Name the blood parasite species.
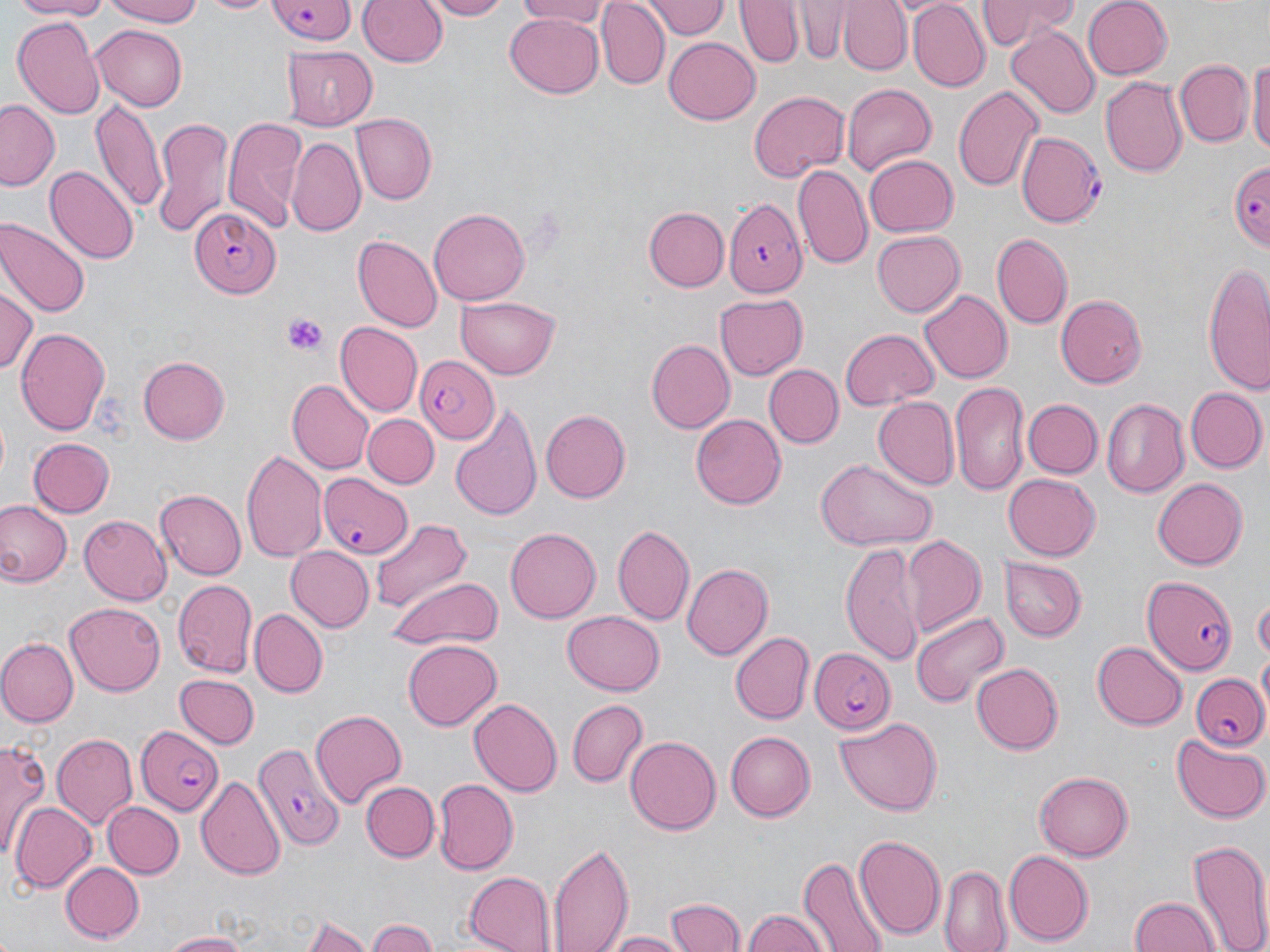
Plasmodium falciparum.

Summary:
  - Coordinate format: approximate bounding boxes as (x1,y1)-(x2,y2) corner pairs in pixels
  - Plasmodium falciparum-infected red blood cell locations: (262,2)-(357,44), (1018,131)-(1106,230), (1225,158)-(1267,252), (727,198)-(808,298), (189,207)-(279,295), (414,355)-(499,444), (319,474)-(413,558), (1144,575)-(1235,674), (807,649)-(895,731), (1189,671)-(1270,750), (136,724)-(225,815), (251,737)-(343,848)
  - Platelet locations: (282,313)-(330,356)
  - Uninfected red blood cell locations: (7,0)-(113,19), (101,0)-(208,26), (196,0)-(276,14), (358,0)-(448,70), (421,0)-(515,20), (514,0)-(616,26), (647,0)-(729,42), (735,0)-(803,68), (839,0)-(913,75), (976,0)-(1078,49), (1080,0)-(1172,81), (907,1)-(989,91), (787,3)-(854,62), (598,4)-(668,88), (506,11)-(604,96), (12,14)-(105,117), (92,23)-(187,109), (1007,26)-(1099,119), (663,38)-(760,124), (282,46)-(374,128), (1248,51)-(1270,165), (1174,59)-(1254,147), (1101,76)-(1188,176), (841,83)-(937,174), (953,83)-(1043,195), (750,90)-(847,184), (91,99)-(165,216), (0,101)-(62,191), (352,115)-(437,203), (222,116)-(307,232), (150,117)-(233,237), (287,137)-(366,238), (865,156)-(959,237), (45,166)-(138,265), (793,166)-(874,272), (644,206)-(729,291), (429,208)-(531,304), (0,218)-(87,320), (871,231)-(964,318), (993,234)-(1073,328), (352,235)-(441,331), (1202,262)-(1270,395), (0,285)-(36,375), (919,289)-(1011,382), (1057,292)-(1148,387), (713,294)-(808,379), (454,297)-(562,379), (334,322)-(422,417), (14,327)-(111,436), (838,327)-(939,409), (646,338)-(734,432), (138,356)-(230,444), (765,364)-(843,447), (287,380)-(372,474), (950,382)-(1029,493), (1186,387)-(1267,472), (873,396)-(959,491), (1102,398)-(1190,497), (1022,399)-(1101,479), (449,406)-(544,521), (539,410)-(629,503), (363,414)-(437,487), (691,415)-(784,508), (27,437)-(113,518), (241,447)-(326,562), (814,461)-(939,552), (1003,472)-(1101,562), (1152,475)-(1247,567), (154,489)-(245,579), (1,502)-(71,587), (78,513)-(172,603), (371,518)-(468,615), (612,525)-(694,626), (506,528)-(600,623), (900,533)-(985,635), (839,540)-(924,664), (284,547)-(371,632), (999,557)-(1088,642), (682,562)-(772,659), (389,575)-(505,651), (171,579)-(258,680), (1253,595)-(1270,659), (65,604)-(165,695), (251,608)-(326,696), (910,609)-(1008,712), (561,610)-(665,695), (728,631)-(813,726), (1,637)-(77,726), (402,639)-(502,730), (1091,640)-(1186,730), (971,661)-(1063,754), (174,674)-(259,750), (468,696)-(561,794), (565,696)-(649,789), (311,709)-(405,808), (835,716)-(945,816), (724,729)-(814,819), (52,732)-(137,828), (1169,734)-(1270,824), (625,736)-(720,836), (2,739)-(52,860), (1033,771)-(1134,862), (197,776)-(283,881), (431,778)-(519,873), (361,780)-(437,862), (104,801)-(183,879), (11,802)-(97,894), (853,834)-(944,941), (1187,837)-(1270,952), (548,839)-(633,952), (1004,848)-(1092,945), (798,858)-(892,952), (59,861)-(144,943), (940,866)-(1013,952), (463,870)-(556,952), (664,895)-(746,952), (1130,896)-(1220,952), (740,910)-(831,952), (302,915)-(373,951), (367,917)-(441,952), (600,929)-(693,951), (161,930)-(251,951)
  - Field of view: single
  - Modality: optical microscopy
  - Image size: 1270×952 pixels
  - Magnification: 1000x
  - Preparation: thin blood film
  - Stain: May-Grünwald-Giemsa